Give the extent of all Plasmodium ovale-infected red blood cells.
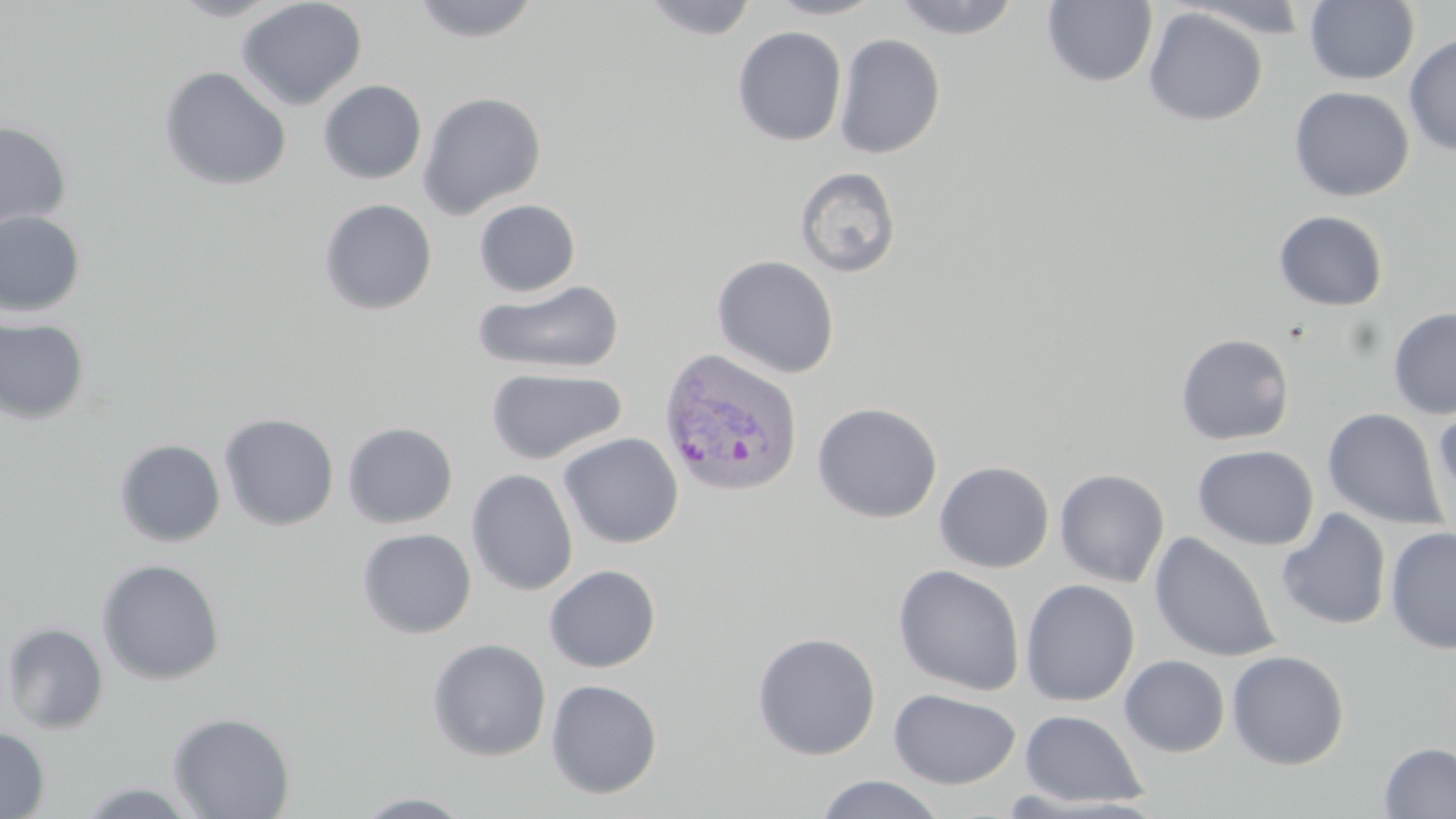
Approximate bounding boxes as (x1, y1, x2, y2) in pixels.
Plasmodium ovale-infected red blood cells: (659, 347, 804, 498).

Uninfected red blood cell locations: (167, 0, 289, 21), (236, 0, 368, 111), (410, 0, 542, 43), (641, 0, 758, 41), (765, 0, 886, 20), (892, 0, 1023, 40), (1304, 0, 1419, 85), (1042, 1, 1158, 88), (1177, 2, 1317, 40), (1143, 7, 1268, 126), (732, 26, 847, 147), (833, 33, 946, 159), (1403, 33, 1456, 156), (158, 66, 292, 191), (318, 80, 427, 184), (1288, 86, 1414, 201), (417, 91, 547, 219), (443, 116, 561, 274), (0, 121, 72, 231), (795, 167, 901, 278), (318, 198, 438, 315), (473, 199, 581, 297), (0, 209, 86, 318), (1273, 210, 1389, 311), (712, 255, 840, 379), (474, 278, 626, 375), (1388, 308, 1456, 419), (0, 317, 91, 426), (1175, 332, 1295, 445), (485, 367, 627, 465), (1434, 399, 1456, 522), (812, 402, 942, 523), (1322, 407, 1447, 530), (218, 412, 339, 531), (341, 422, 458, 528), (558, 432, 684, 549), (114, 438, 226, 547), (1192, 444, 1319, 550), (934, 460, 1055, 573), (466, 468, 579, 596), (1055, 468, 1170, 588), (1276, 508, 1391, 630), (1385, 526, 1455, 654), (356, 528, 477, 638), (1149, 532, 1281, 663), (96, 558, 226, 686), (543, 564, 662, 672), (892, 564, 1026, 696), (1020, 579, 1140, 707), (1, 621, 109, 734), (751, 631, 881, 760), (427, 638, 551, 761), (1227, 649, 1350, 770), (1120, 654, 1230, 757), (545, 678, 663, 799), (888, 688, 1021, 789), (1019, 709, 1148, 808), (168, 711, 296, 819), (0, 727, 51, 818), (1378, 742, 1456, 818), (815, 774, 946, 818), (75, 780, 205, 817), (353, 791, 476, 818). Slide-level diagnosis: Plasmodium ovale. Single field of view. 1000x magnification. May-Grünwald-Giemsa-stained preparation. Image is 1456×819 pixels. Optical microscopy. Thin blood smear.